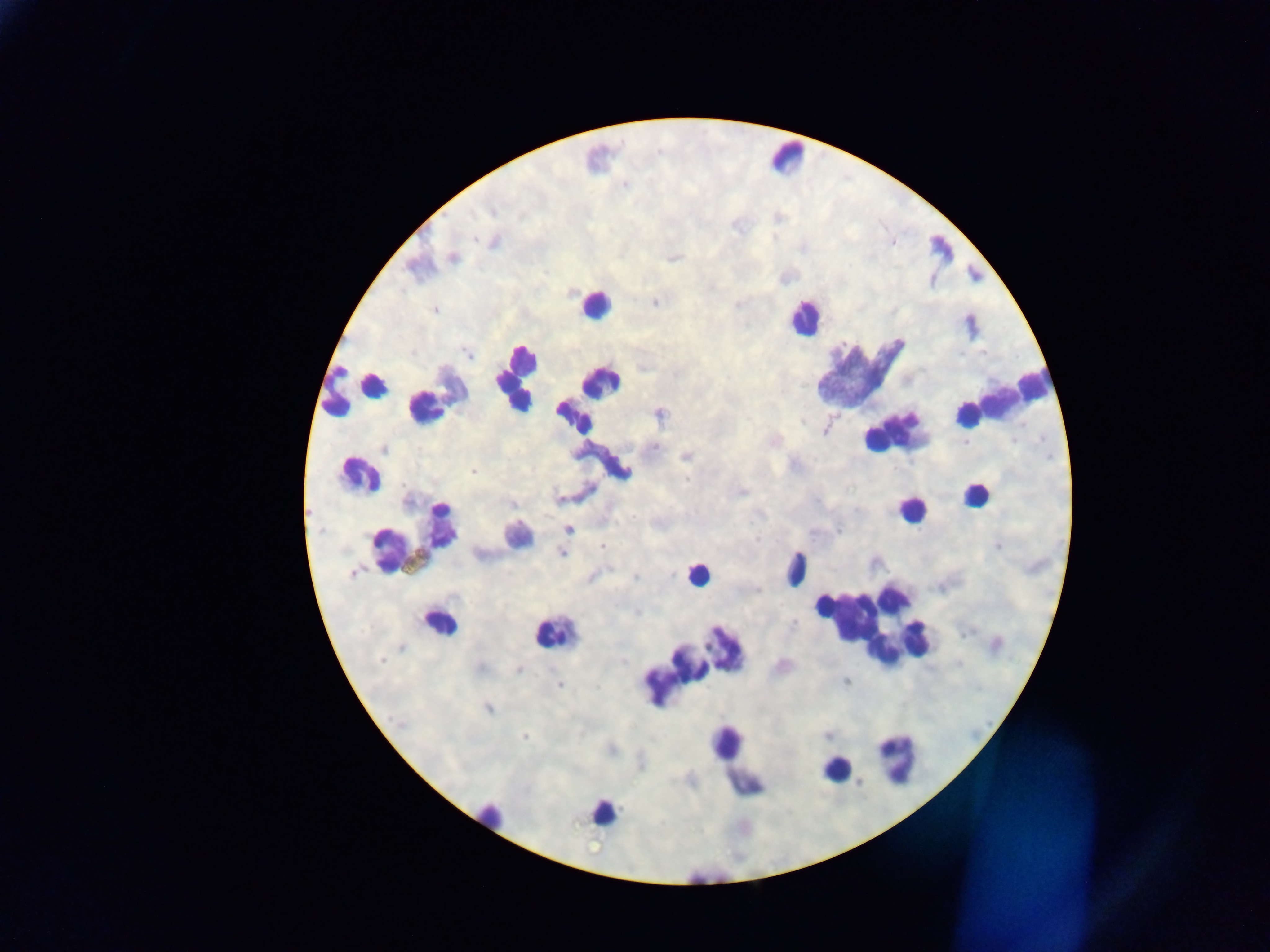

field_of_view: single
leukocyte_locations: 'approximate centers as (x, y) in pixels: (786, 158), (594, 306), (805, 318), (860, 376), (515, 378), (356, 388), (590, 394), (997, 400), (423, 406), (893, 426), (358, 474), (975, 497), (909, 510), (515, 536), (419, 540), (796, 568), (697, 575), (441, 617), (868, 623), (551, 633), (692, 663), (896, 758), (737, 762), (836, 769), (492, 814), (599, 816)'
capture: mobile-phone photograph through a microscope
country: Ghana
preparation: thick blood film
image_size: 1270×952 pixels
plasmodium_parasite_locations: 'approximate centers as (x, y) in pixels: (453, 256), (654, 303), (435, 310), (655, 446), (384, 449), (686, 457), (472, 472), (742, 491), (558, 499), (633, 517), (569, 529), (602, 546), (561, 554), (352, 573), (381, 660), (519, 671), (559, 685), (488, 709), (525, 736)'